Describe the morphology of the red blood cells.
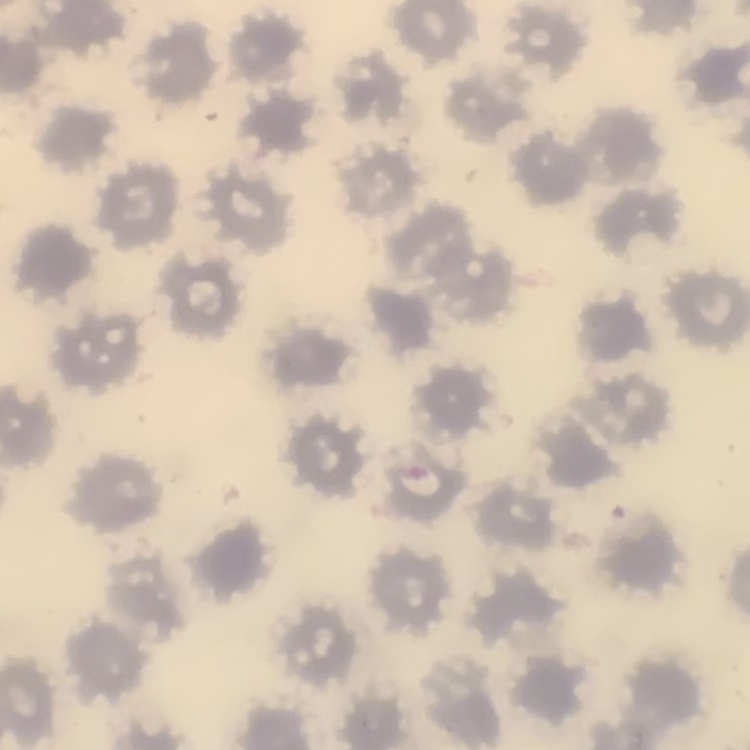

No rouleaux formation.

Summary:
  - Image type: one tile cut from a larger photomicrograph
  - Stain: Field's or Giemsa
  - Preparation: thin peripheral smear